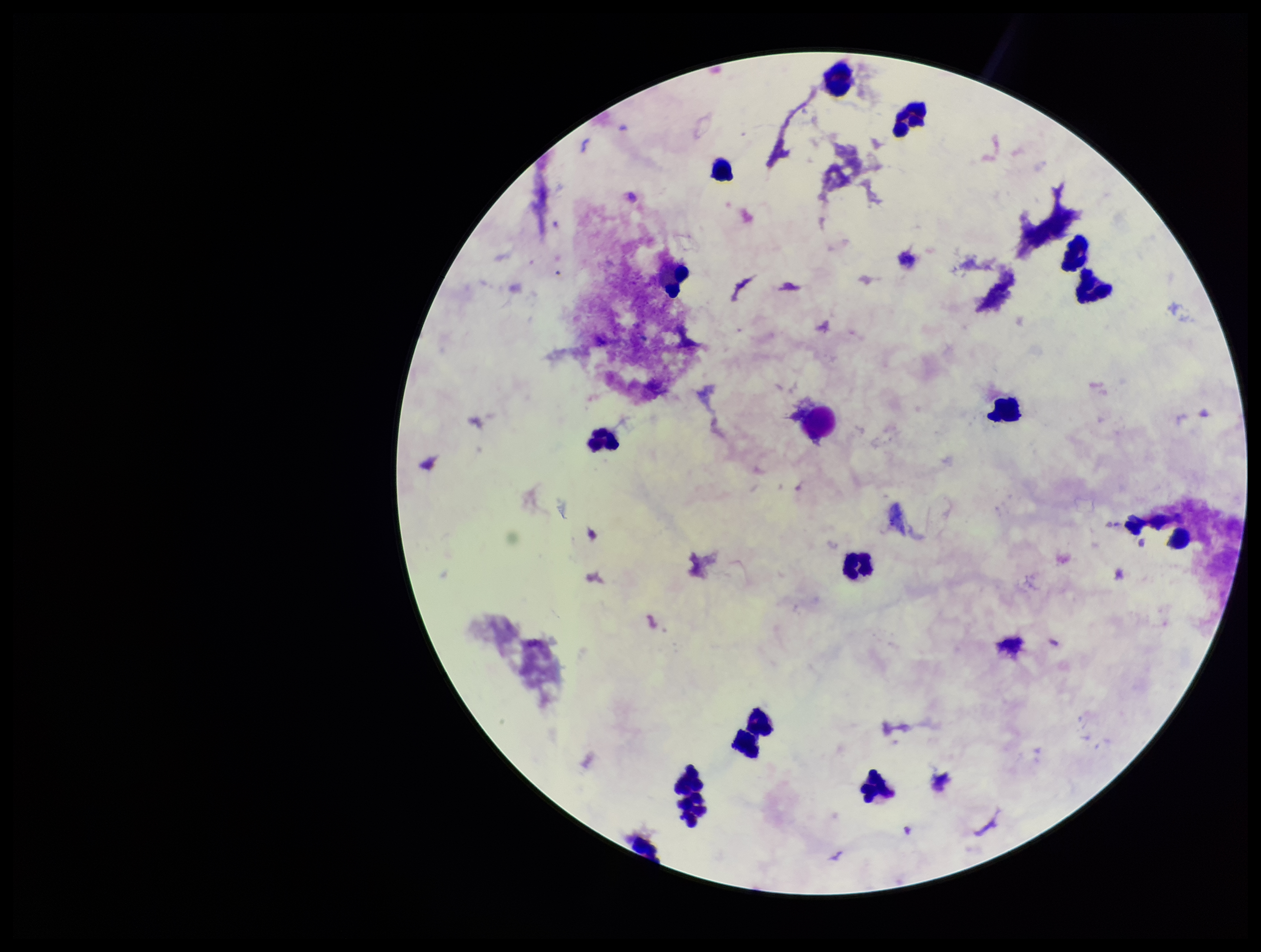

Summary:
  - Parasite count: 0
  - Patient malaria status: negative
  - Leukocyte count: 15
  - Image size: 1261×952 pixels
  - Stain: Giemsa
  - Field of view: one from this slide
  - Capture: smartphone photograph through the microscope eyepiece
  - Plasmodium parasites: none identified
  - Preparation: thick blood smear